State which parasite is depicted.
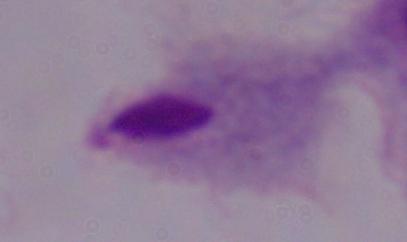
This is a trichomonad.

1000x magnification. Photomicrograph.